Comment on the morphology of the erythrocytes.
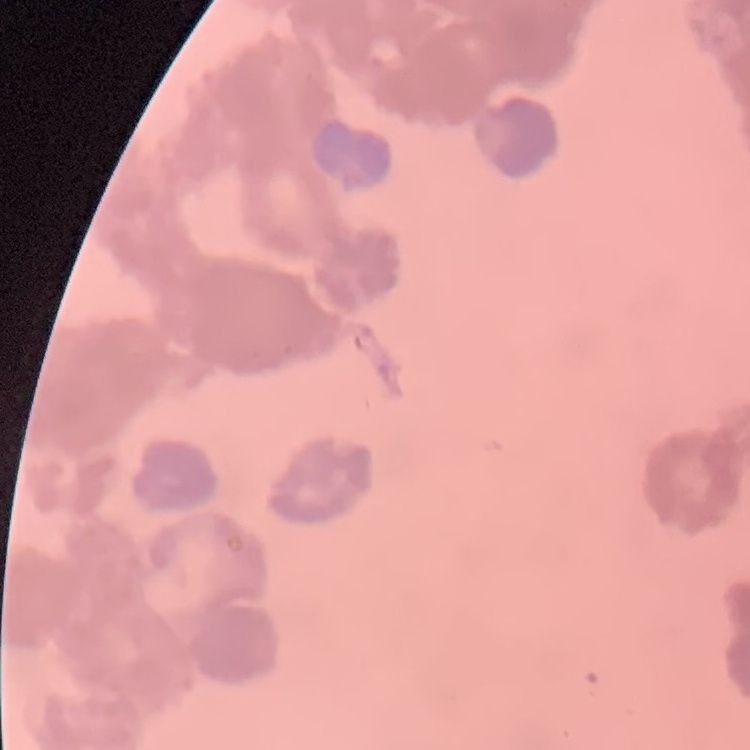
Rouleaux formation.

stain = Field's or Giemsa
image type = square crop of a larger photomicrograph
preparation = thin blood smear